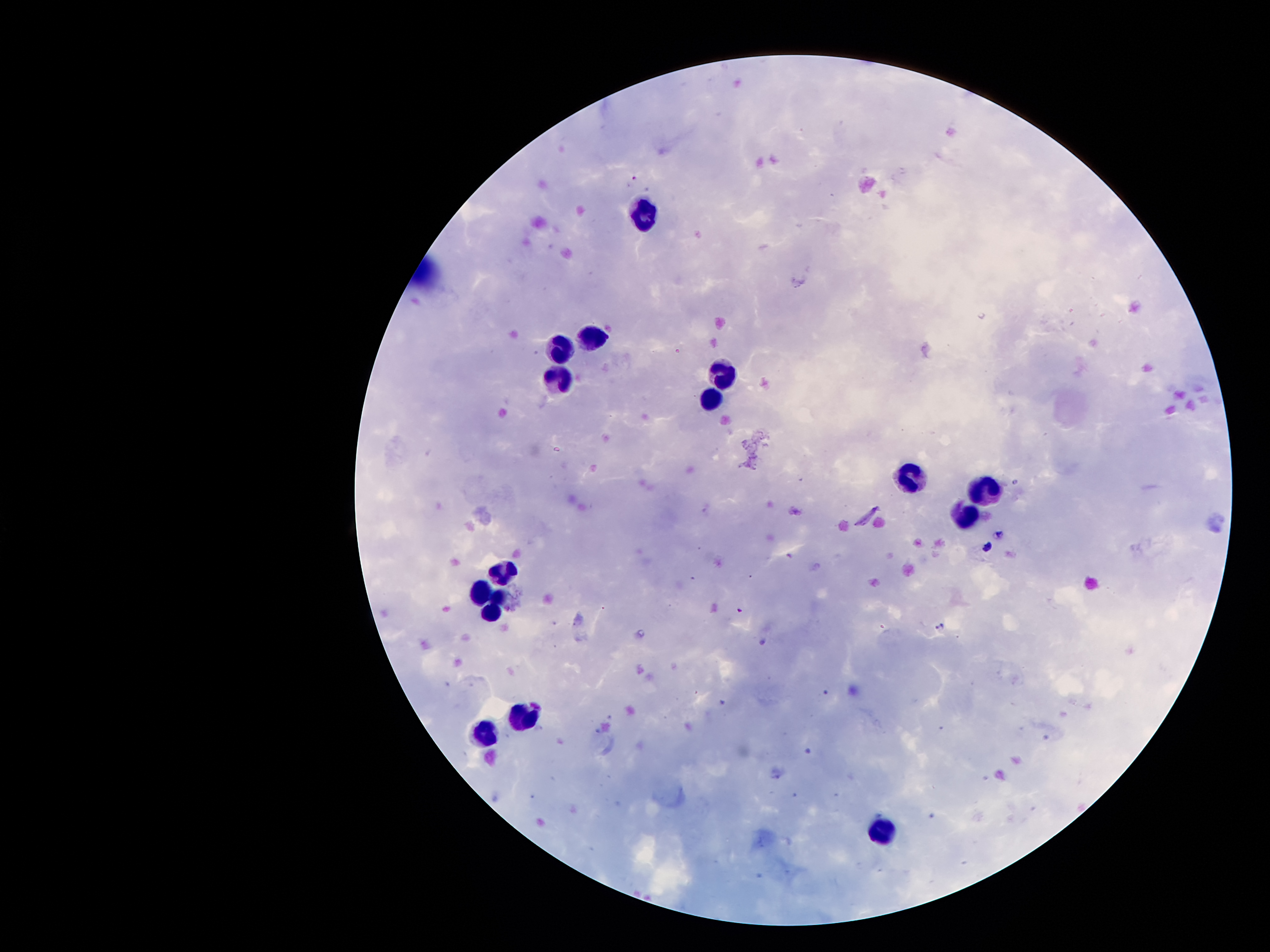

Approximate centers as (x, y) in pixels.
Summary:
  - Plasmodium parasite locations: (635, 179), (1000, 534), (986, 547), (941, 627)
  - Leukocyte locations: (643, 214), (590, 335), (559, 343), (727, 377), (553, 379), (709, 400), (915, 479), (990, 487), (964, 517), (503, 572), (483, 591), (501, 598), (490, 610), (522, 715), (487, 735), (882, 829)
  - Patient malaria status: infected with Plasmodium falciparum
  - Capture: smartphone camera through the microscope eyepiece
  - Magnification: 100x
  - Stain: Giemsa
  - Image size: 1270×952 pixels
  - Preparation: thick blood smear
  - Field of view: single